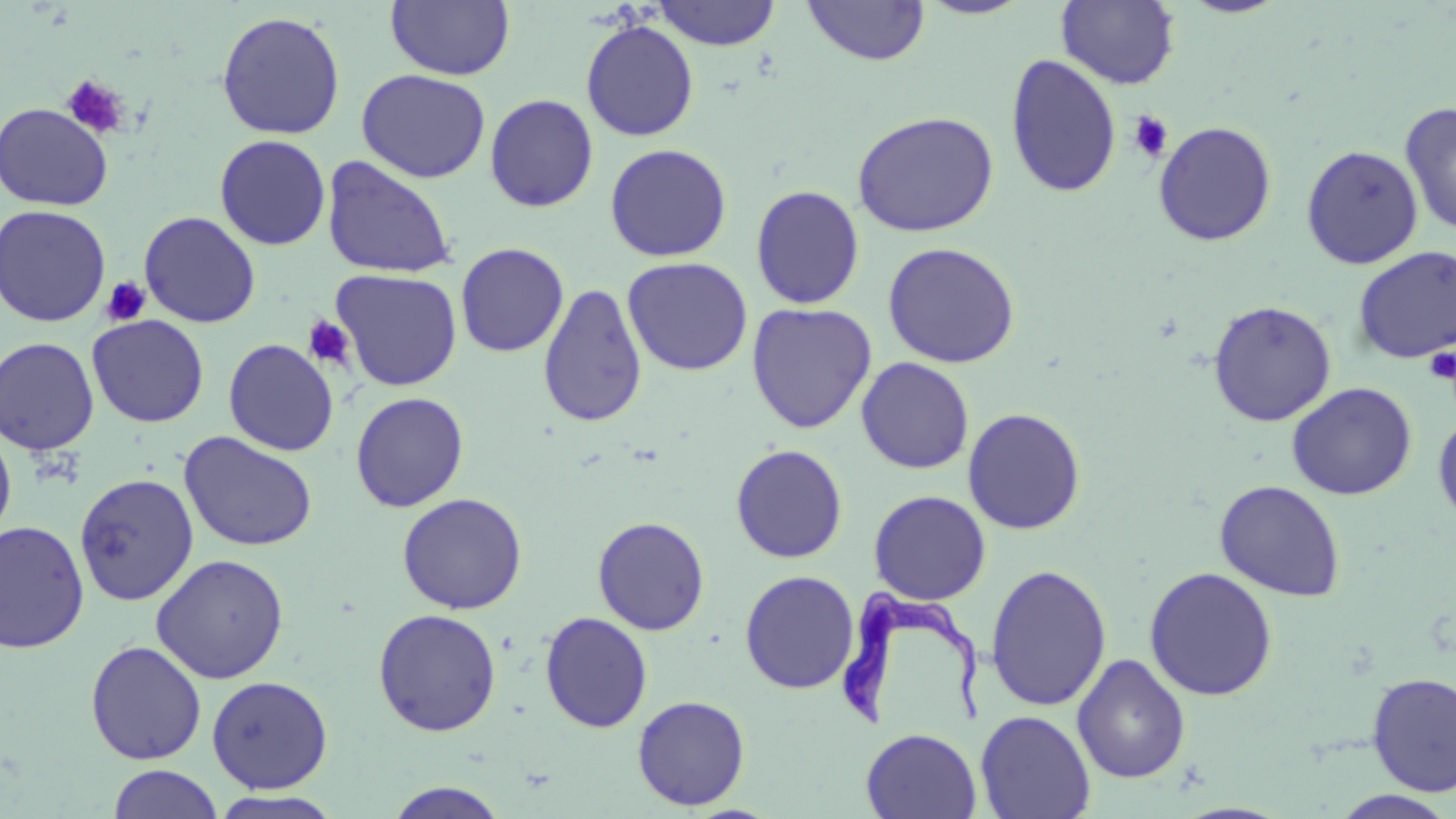

Summary:
  - Coordinate format: approximate bounding boxes as [x1, y1, x2, y2] in pixels
  - Trypanosoma brucei locations: [832, 586, 988, 737]
  - Platelet locations: [61, 74, 130, 139], [1129, 110, 1173, 163], [101, 276, 151, 327], [301, 315, 356, 370], [1423, 346, 1456, 385]
  - Uninfected red blood cell locations: [385, 0, 515, 80], [916, 0, 1036, 20], [1056, 0, 1181, 89], [1177, 0, 1292, 18], [652, 1, 782, 50], [802, 1, 930, 66], [216, 10, 345, 140], [580, 19, 699, 141], [1005, 53, 1122, 198], [356, 68, 491, 183], [484, 93, 599, 213], [0, 102, 114, 212], [1400, 102, 1456, 237], [852, 111, 999, 237], [1153, 121, 1277, 246], [214, 134, 331, 250], [604, 143, 732, 262], [1301, 144, 1424, 269], [321, 155, 457, 279], [750, 184, 865, 310], [0, 204, 112, 327], [139, 211, 261, 328], [882, 241, 1021, 369], [455, 242, 569, 357], [1352, 246, 1456, 365], [621, 257, 753, 376], [331, 269, 462, 391], [538, 283, 648, 427], [1208, 300, 1337, 426], [746, 302, 877, 434], [87, 314, 209, 427], [0, 336, 99, 455], [223, 338, 339, 456], [856, 357, 975, 474], [1287, 382, 1417, 501], [350, 391, 469, 512], [962, 407, 1086, 535], [1433, 414, 1456, 526], [0, 420, 16, 547], [180, 432, 318, 552], [730, 443, 848, 563], [74, 473, 199, 606], [1214, 480, 1347, 601], [868, 490, 992, 605], [397, 492, 527, 614], [592, 516, 710, 635], [0, 520, 90, 653], [150, 553, 289, 684], [985, 563, 1112, 713], [1144, 566, 1279, 701], [739, 570, 859, 694], [373, 608, 502, 737], [539, 611, 653, 733], [85, 640, 207, 765], [1072, 653, 1191, 783], [1366, 672, 1456, 797], [206, 675, 333, 793], [632, 695, 751, 810], [975, 710, 1096, 819], [861, 728, 982, 818], [107, 764, 223, 819], [383, 781, 511, 818], [209, 790, 345, 819], [1330, 790, 1455, 819]
  - Slide-level diagnosis: Trypanosoma brucei
  - Modality: light microscopy
  - Field of view: one of a larger specimen
  - Image size: 1456×819 pixels
  - Preparation: thin blood film
  - Magnification: 1000x
  - Stain: May-Grünwald-Giemsa